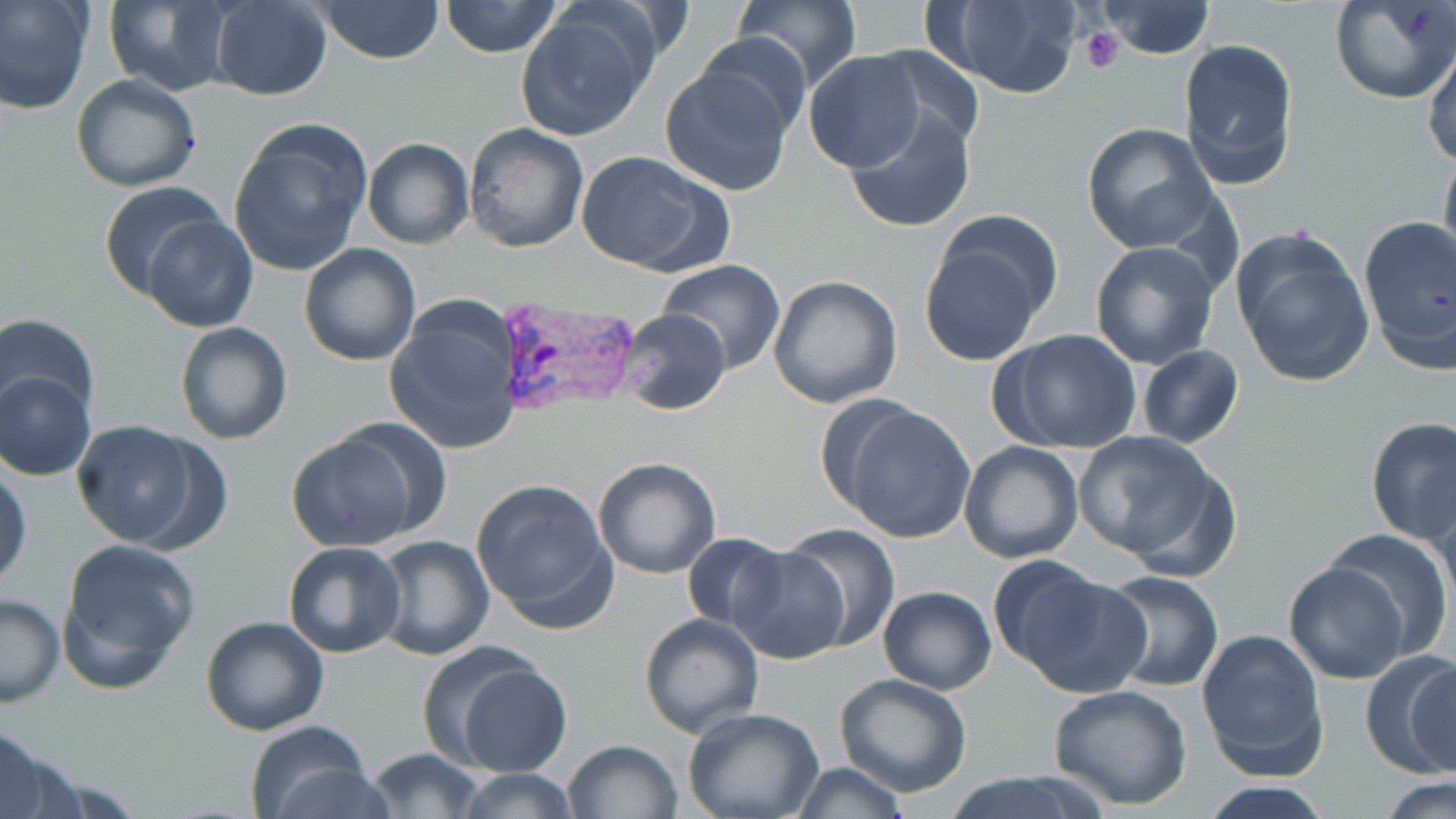
Approximate bounding boxes as (x1,y1)-(x2,y2) corner pairs in pixels. Plasmodium vivax-infected red blood cell locations: (494,295)-(641,419). Uninfected red blood cell locations: (0,0)-(94,115), (315,0)-(445,64), (440,0)-(563,58), (732,0)-(861,92), (930,0)-(1085,98), (101,1)-(234,95), (209,1)-(332,100), (1093,1)-(1215,59), (1329,1)-(1456,105), (515,7)-(657,141), (693,34)-(812,137), (1177,37)-(1299,191), (1423,43)-(1456,168), (868,45)-(985,152), (804,50)-(925,172), (658,67)-(796,197), (70,74)-(201,191), (844,109)-(976,234), (228,121)-(373,276), (462,121)-(589,252), (1080,122)-(1218,253), (362,137)-(474,249), (1439,144)-(1456,273), (574,150)-(732,275), (98,181)-(227,301), (141,213)-(260,332), (1357,215)-(1456,368), (918,225)-(1053,367), (1230,228)-(1376,389), (1089,241)-(1221,370), (298,243)-(421,366), (656,261)-(787,372), (767,275)-(902,410), (384,303)-(523,455), (617,309)-(730,415), (3,312)-(99,431), (174,322)-(292,444), (990,328)-(1142,454), (1137,345)-(1243,449), (1,369)-(95,481), (836,403)-(978,542), (1364,416)-(1456,545), (72,421)-(208,549), (284,430)-(428,553), (1073,430)-(1225,567), (959,440)-(1084,564), (592,457)-(721,580), (0,463)-(33,589), (472,479)-(618,631), (1430,488)-(1456,617), (783,525)-(900,651), (1322,529)-(1454,659), (680,532)-(791,633), (368,535)-(495,661), (57,539)-(201,692), (283,542)-(408,658), (726,545)-(852,664), (675,557)-(814,698), (1284,563)-(1412,685), (1005,565)-(1151,698), (1096,570)-(1224,693), (877,586)-(997,695), (0,593)-(65,706), (638,613)-(765,738), (200,615)-(330,736), (1195,627)-(1329,779), (422,645)-(572,776), (1361,650)-(1456,780), (834,673)-(972,797), (1047,683)-(1193,810), (682,709)-(825,819), (244,725)-(381,819), (0,733)-(80,819), (562,739)-(684,819), (366,748)-(484,818), (787,763)-(912,818), (451,768)-(584,819), (942,771)-(1107,819), (1377,776)-(1456,818), (1194,780)-(1337,817). Platelet locations: (1079,27)-(1126,73). Slide-level diagnosis: Plasmodium vivax. Thin blood film. May-Grünwald-Giemsa stain. Image is 1456×819 pixels. 1000x magnification. Light microscopy. One field of a larger specimen.